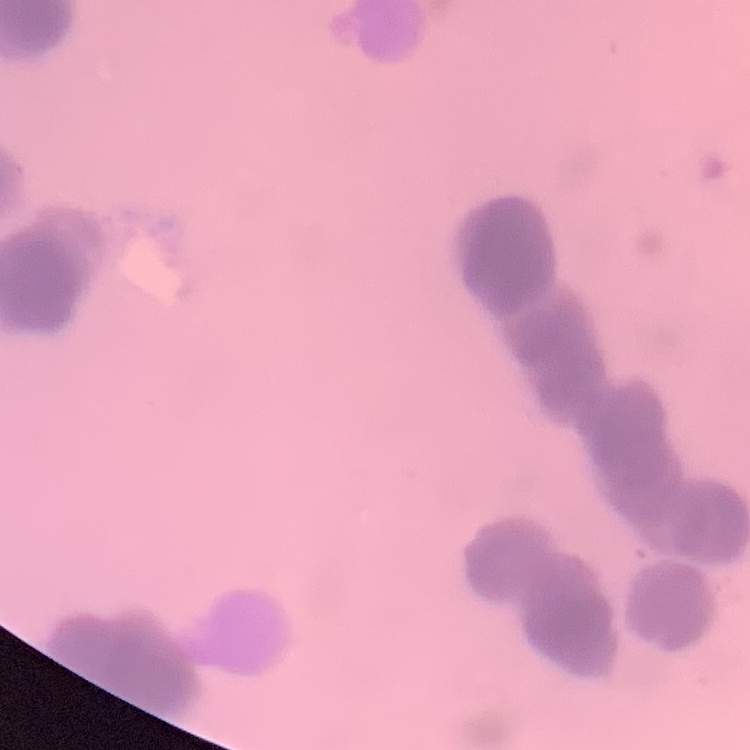
red blood cell morphology = rouleaux formation
preparation = thin blood smear
image type = square crop of a larger photomicrograph
stain = Field's or Giemsa